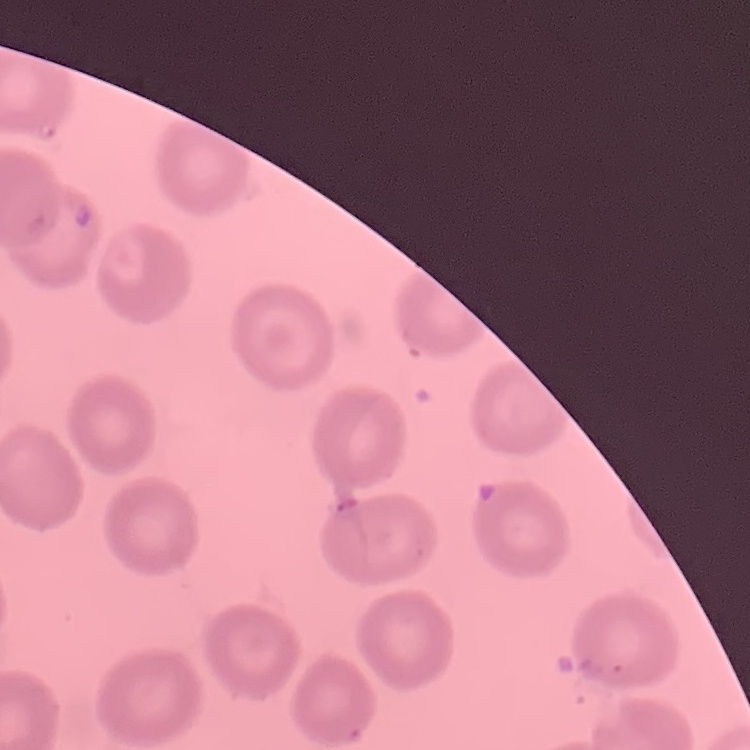

red blood cell morphology = no rouleaux formation
preparation = thin peripheral smear
image type = one tile cut from a larger photomicrograph
stain = Field's or Giemsa